State which cell type is depicted.
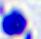

A leukocyte.

modality: micrograph
magnification: 400x